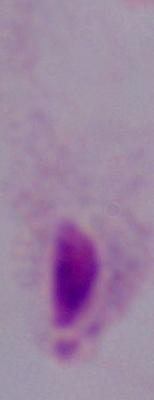

magnification = 1000x
modality = photomicrograph
identification = trichomonad